Report the malaria status of this cell.
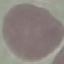

It is uninfected.

capture = smartphone camera at the microscope eyepiece
stain = Giemsa
preparation = thin smear
image type = automatically extracted cell patch, resized to 64 × 64 pixels